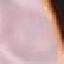

Summary:
  - Malaria status: uninfected
  - Stain: Giemsa
  - Image type: cell patch, automatically extracted from a larger field of view and resized to 64 × 64 pixels
  - Preparation: thin blood film
  - Capture: smartphone through the microscope eyepiece